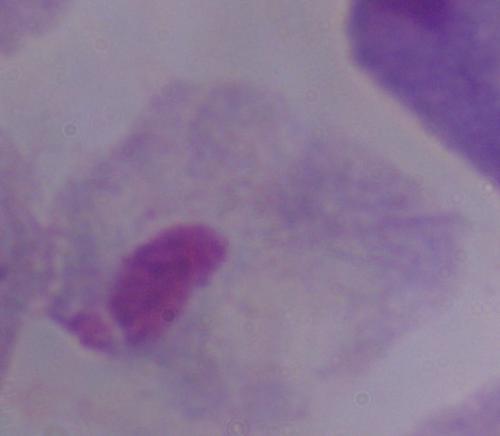 Photomicrograph. Captured at 1000x magnification. A trichomonad is seen.